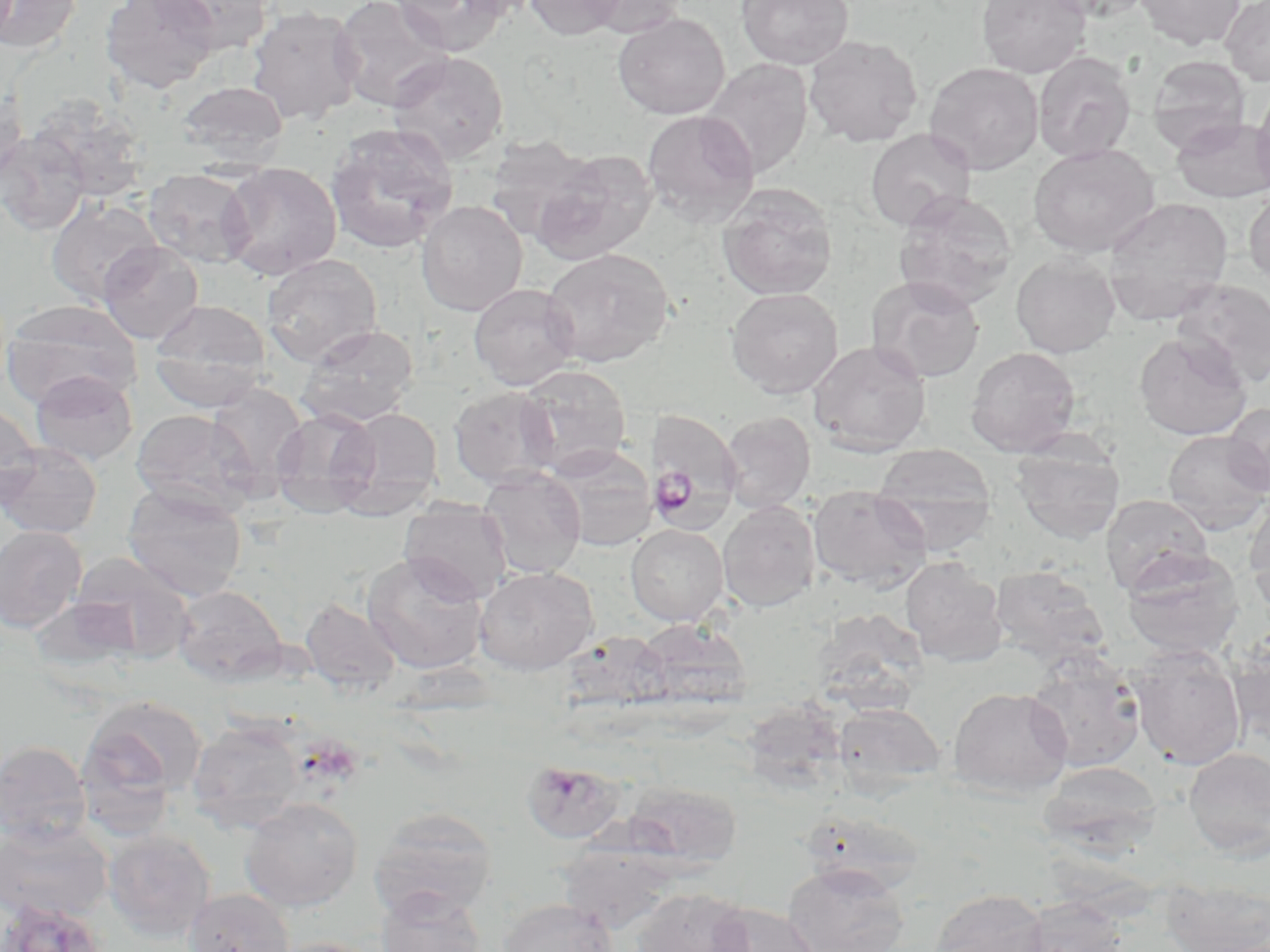
{
  "plasmodium_ovale_infected_red_blood_cell_locations": "approximate bounding boxes as (x1,y1)-(x2,y2) corner pairs in pixels: (647,408)-(744,528)",
  "slide_level_diagnosis": "Plasmodium ovale",
  "uninfected_red_blood_cell_locations": "approximate bounding boxes as (x1,y1)-(x2,y2) corner pairs in pixels: (0,0)-(83,54), (99,0)-(221,94), (150,0)-(274,54), (331,0)-(453,112), (390,0)-(511,54), (451,0)-(542,21), (524,0)-(627,40), (581,0)-(688,38), (736,0)-(854,70), (976,0)-(1092,78), (1042,0)-(1153,21), (1136,0)-(1245,50), (1220,0)-(1270,86), (246,6)-(365,126), (612,12)-(730,119), (803,34)-(923,147), (385,51)-(509,165), (1033,52)-(1137,163), (1148,55)-(1251,154), (701,58)-(814,177), (924,62)-(1044,175), (177,80)-(289,167), (1252,80)-(1270,200), (0,86)-(28,196), (25,95)-(152,203), (641,109)-(760,226), (1172,117)-(1270,203), (325,123)-(459,254), (865,128)-(977,230), (0,129)-(90,236), (483,134)-(598,242), (1028,143)-(1159,258), (530,148)-(659,265), (219,162)-(342,280), (143,169)-(256,269), (717,185)-(838,301), (1243,188)-(1270,285), (893,191)-(1018,310), (1102,196)-(1233,324), (46,197)-(163,306), (416,200)-(527,316), (97,241)-(203,344), (541,247)-(674,368), (1010,252)-(1121,358), (261,254)-(383,367), (867,276)-(985,383), (1172,278)-(1270,389), (468,282)-(580,389), (726,287)-(843,398), (2,299)-(142,407), (148,299)-(271,409), (297,324)-(419,428), (1133,332)-(1253,440), (807,340)-(931,456), (964,346)-(1081,457), (516,364)-(632,476), (30,370)-(138,466), (206,383)-(309,494), (449,387)-(560,489), (0,401)-(41,505), (1222,402)-(1270,497), (336,406)-(443,514), (270,408)-(383,516), (131,409)-(259,516), (720,411)-(816,513), (1162,430)-(1270,535), (1011,438)-(1125,545), (0,442)-(103,540), (543,444)-(658,551), (871,444)-(997,554), (477,467)-(586,579), (123,484)-(247,601), (807,484)-(930,591), (1100,494)-(1213,595), (1244,495)-(1270,612), (718,500)-(821,612), (398,501)-(512,603), (626,524)-(728,626), (0,526)-(87,633), (1121,548)-(1245,661), (362,552)-(490,675), (68,553)-(195,663), (900,556)-(1008,667), (989,565)-(1109,666), (474,566)-(598,674), (172,585)-(288,686), (300,597)-(402,697), (634,618)-(751,713), (1230,627)-(1270,746), (561,631)-(670,713), (1128,646)-(1247,770), (1025,651)-(1147,775), (948,686)-(1072,797), (78,695)-(207,814), (833,703)-(945,795), (187,720)-(306,831), (0,740)-(91,849), (1184,747)-(1270,859), (522,760)-(626,845), (1039,761)-(1163,858), (621,780)-(742,871), (240,798)-(363,912), (369,806)-(499,919), (798,808)-(927,896), (0,820)-(112,924), (103,830)-(216,939), (557,842)-(680,934), (782,862)-(910,952), (1160,876)-(1270,952), (376,886)-(488,952), (630,886)-(756,952), (185,888)-(294,952), (929,888)-(1049,952), (1019,895)-(1129,952), (498,898)-(617,952), (1,899)-(109,952), (709,902)-(822,952), (267,937)-(386,952)",
  "preparation": "thin blood smear",
  "magnification": "1000x",
  "modality": "optical microscopy",
  "field_of_view": "single",
  "image_size": "1270×952 pixels",
  "stain": "May-Grünwald-Giemsa"
}